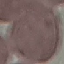

Summary:
  - Result: no malaria parasites seen
  - Stain: Giemsa
  - Image type: cell patch, automatically extracted from a larger field of view and resized to 64 × 64 pixels
  - Preparation: thin blood smear
  - Capture: smartphone camera at the microscope eyepiece